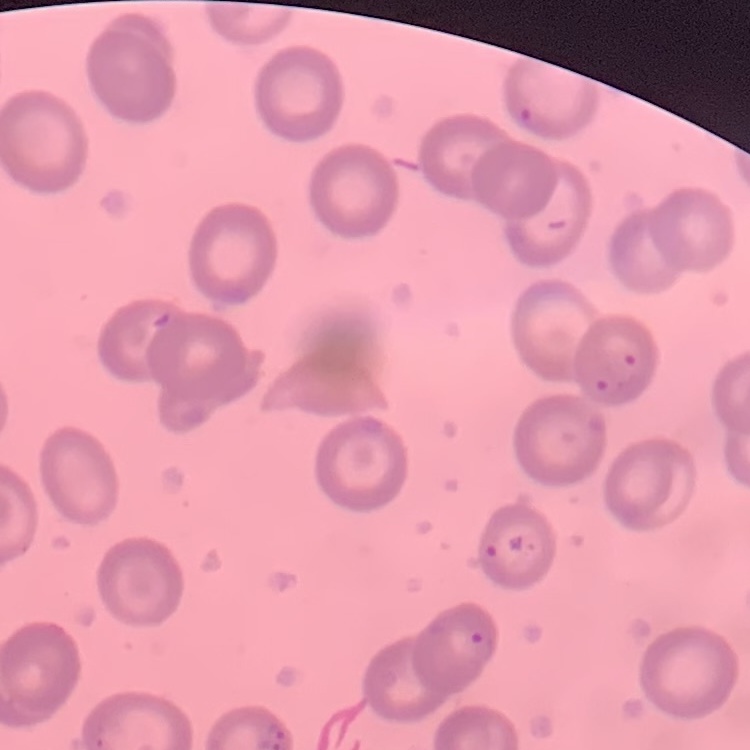
erythrocyte morphology = no rouleaux formation
stain = Field's or Giemsa
preparation = thin blood film
image type = one tile cut from a larger photomicrograph